Outline every trophozoite.
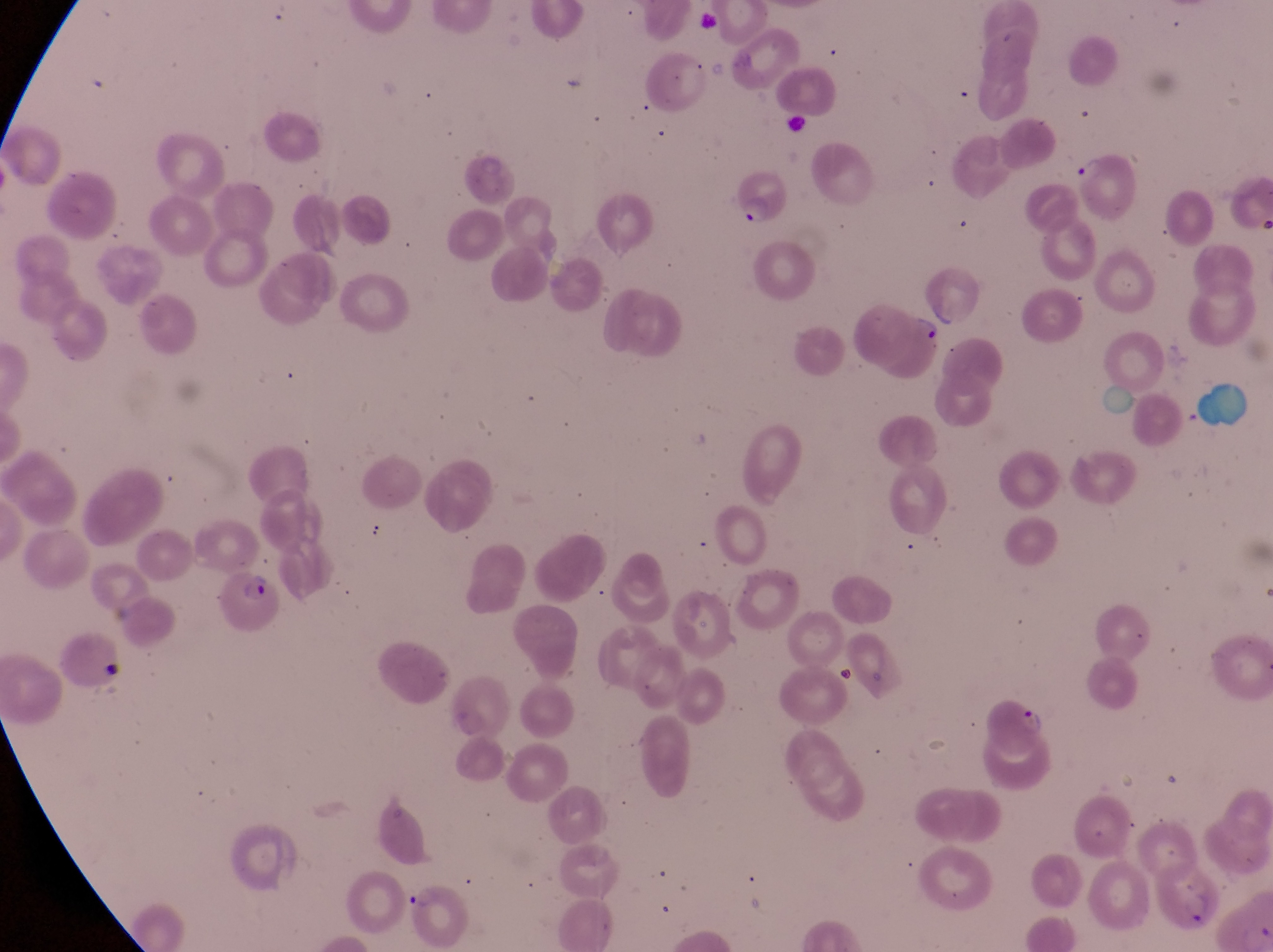
Approximate bounding boxes as [left, top, right, bottom] in pixels.
Trophozoites: [914, 313, 953, 352], [1019, 705, 1051, 740].

Artifact (platelet-like body, stain precipitate, or debris) locations: [781, 110, 814, 138], [100, 658, 126, 677]. Parasitised red blood cell locations: [1068, 150, 1139, 221], [729, 174, 798, 234], [217, 574, 282, 632], [1160, 857, 1220, 929], [402, 878, 476, 952]. Captured by a smartphone held over the eyepiece of an Olympus CX-23 microscope. Magnification of 1000x. Image is 1273×952 pixels. Thin blood smear. Single field of view. Sample from Uganda.